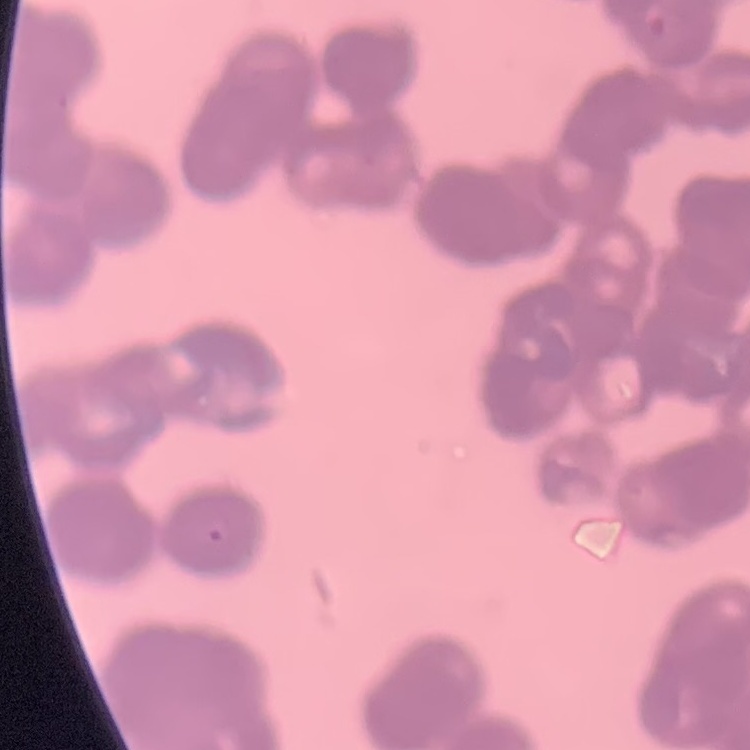

Summary:
  - Erythrocyte morphology: rouleaux formation
  - Stain: Field's or Giemsa
  - Image type: one tile cut from a larger photomicrograph
  - Preparation: thin blood film